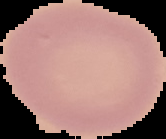 Result: no Plasmodium parasites detected. Cell region segmented out of the field of view; the surrounding area is masked to black. From a thin blood film. Image is 166×139 pixels.